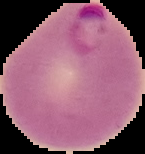 Image is 145×154 pixels. Result: Plasmodium parasites identified. The area outside the segmented cell region is set to black. From a thin blood film.